Locate every uninfected red blood cell.
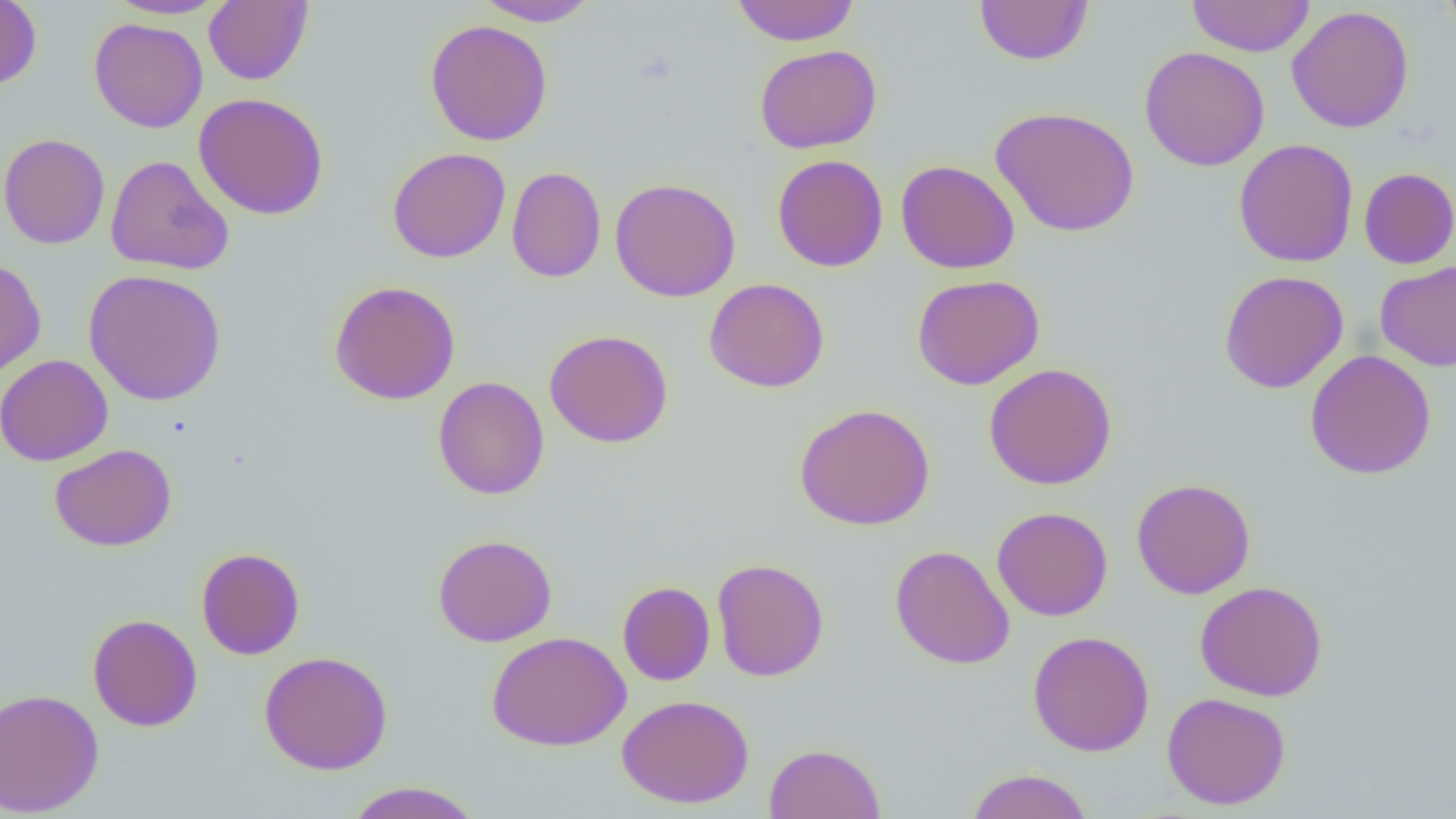
Approximate bounding boxes as [x1, y1, x2, y2] in pixels.
Uninfected red blood cells: [0, 0, 42, 91], [106, 0, 228, 20], [203, 0, 313, 86], [473, 0, 601, 26], [730, 0, 861, 46], [974, 0, 1093, 66], [1186, 0, 1316, 57], [1439, 0, 1456, 42], [1287, 5, 1415, 133], [89, 17, 208, 133], [425, 19, 553, 146], [754, 44, 882, 154], [1139, 46, 1270, 171], [193, 92, 329, 220], [990, 105, 1140, 237], [0, 133, 110, 250], [1233, 138, 1359, 268], [387, 147, 511, 263], [772, 154, 888, 272], [105, 155, 233, 275], [895, 159, 1020, 274], [506, 166, 607, 283], [1358, 167, 1456, 269], [610, 177, 741, 302], [0, 256, 47, 379], [1375, 260, 1456, 372], [83, 269, 227, 406], [1218, 270, 1349, 394], [912, 274, 1045, 390], [704, 278, 830, 393], [329, 280, 461, 405], [544, 329, 673, 448], [1304, 350, 1437, 480], [0, 354, 113, 466], [984, 363, 1117, 490], [432, 376, 549, 499], [794, 403, 935, 531], [49, 443, 177, 552], [1131, 478, 1256, 599], [992, 506, 1113, 622], [432, 534, 557, 647], [890, 545, 1015, 669], [196, 547, 305, 660], [712, 558, 829, 682], [617, 580, 716, 685], [1195, 580, 1328, 701], [87, 613, 203, 731], [1028, 630, 1155, 757], [486, 631, 630, 751], [259, 650, 393, 775], [0, 688, 104, 816], [1162, 691, 1291, 810], [616, 693, 755, 809], [764, 742, 886, 819], [965, 768, 1093, 819], [344, 781, 485, 819].

Summary:
  - Slide-level diagnosis: no evidence of blood parasites
  - Field of view: one of a larger specimen
  - Magnification: 1000x
  - Modality: light microscopy
  - Preparation: thin blood smear
  - Image size: 1456×819 pixels